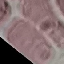

Result: no malaria parasites seen. Acquired by smartphone through the microscope eyepiece. Cell patch, automatically extracted from a larger field of view and resized to 64 × 64 pixels. Thin blood smear. Giemsa-stained preparation.